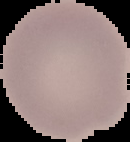
Summary:
  - Result: negative for malaria parasites
  - Image type: cell region segmented out of the field of view; surrounding area masked to black
  - Image size: 130×142 pixels
  - Preparation: thin blood smear